Give the extent of all Plasmodium falciparum-infected red blood cells.
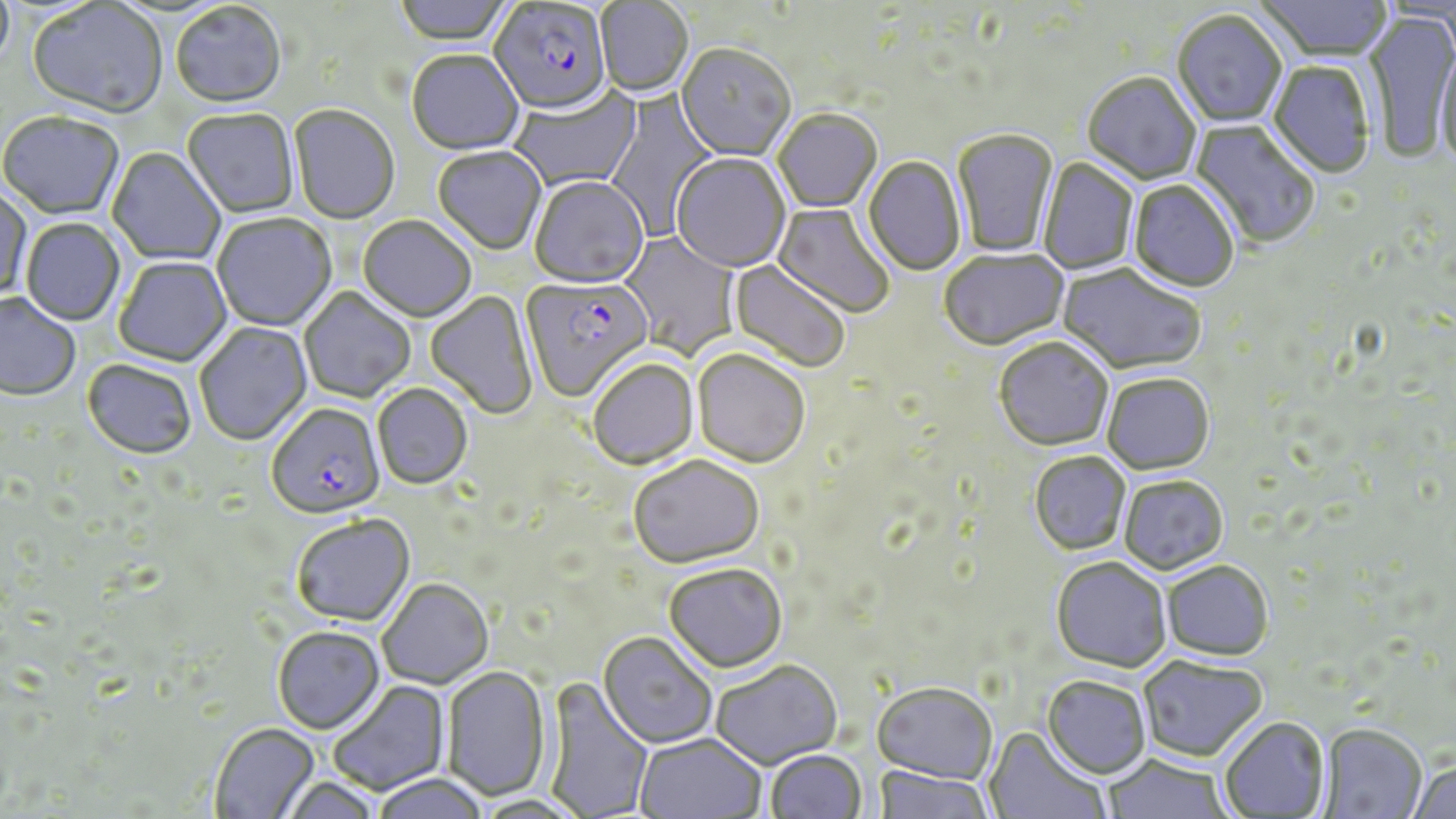

Approximate bounding boxes as [x1, y1, x2, y2] in pixels.
Plasmodium falciparum-infected red blood cells: [489, 2, 613, 119], [520, 276, 653, 404], [267, 405, 385, 521].

Uninfected red blood cell locations: [393, 0, 515, 48], [1255, 0, 1392, 64], [596, 1, 694, 98], [27, 2, 168, 122], [170, 4, 287, 111], [1172, 12, 1287, 130], [1364, 12, 1455, 166], [1435, 41, 1455, 176], [675, 46, 796, 163], [407, 52, 524, 157], [1267, 62, 1375, 180], [1081, 74, 1202, 187], [508, 86, 644, 192], [604, 88, 720, 239], [288, 106, 400, 227], [182, 110, 300, 219], [773, 110, 882, 214], [0, 114, 124, 221], [1188, 120, 1319, 251], [951, 130, 1059, 258], [107, 148, 226, 266], [433, 148, 547, 256], [671, 155, 791, 275], [863, 157, 965, 277], [1039, 157, 1139, 275], [529, 178, 649, 292], [1127, 180, 1239, 295], [0, 186, 33, 302], [770, 202, 895, 319], [212, 215, 337, 332], [358, 217, 476, 324], [21, 219, 125, 326], [618, 229, 742, 361], [939, 251, 1069, 353], [113, 258, 232, 368], [728, 259, 850, 373], [1056, 264, 1206, 378], [299, 287, 415, 404], [425, 291, 538, 420], [0, 294, 80, 402], [194, 322, 313, 447], [994, 339, 1113, 454], [691, 351, 810, 471], [82, 361, 197, 462], [588, 361, 699, 472], [1102, 375, 1214, 477], [373, 385, 473, 491], [1029, 453, 1131, 556], [628, 457, 764, 571], [1118, 477, 1228, 577], [291, 516, 415, 628], [1050, 559, 1172, 675], [1162, 563, 1274, 663], [663, 566, 787, 676], [377, 580, 494, 690], [272, 627, 385, 736], [597, 634, 717, 750], [1137, 657, 1268, 764], [711, 663, 842, 771], [441, 667, 552, 802], [540, 677, 654, 819], [1041, 677, 1151, 781], [329, 680, 450, 795], [871, 684, 997, 786], [1220, 718, 1331, 818], [209, 724, 320, 819], [1316, 726, 1427, 818], [983, 728, 1110, 819], [635, 734, 766, 819], [765, 751, 867, 818], [1100, 756, 1232, 818], [1408, 760, 1456, 819], [872, 767, 993, 819], [373, 776, 488, 819], [281, 777, 383, 818], [472, 797, 588, 819]. Slide-level diagnosis: Plasmodium falciparum. Single field of view. Captured at 1000x magnification. Image is 1456×819 pixels. Optical microscopy. Thin blood film. May-Grünwald-Giemsa-stained preparation.